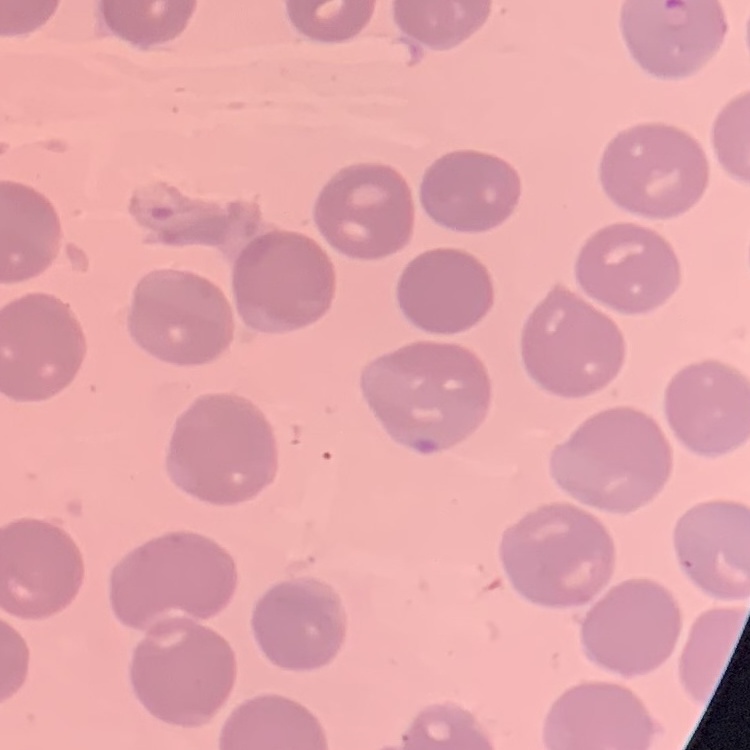

red blood cell morphology = no rouleaux formation
stain = Field's or Giemsa
preparation = thin peripheral smear
image type = one tile cut from a larger photomicrograph